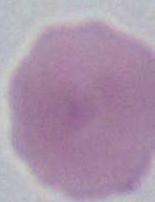

magnification = 1000x
modality = photomicrograph
identification = erythrocyte